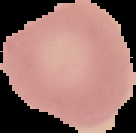

Summary:
  - Malaria status: uninfected
  - Preparation: thin blood film
  - Image type: segmented cell region with the area outside set to black
  - Image size: 136×133 pixels